Point out each Plasmodium parasite.
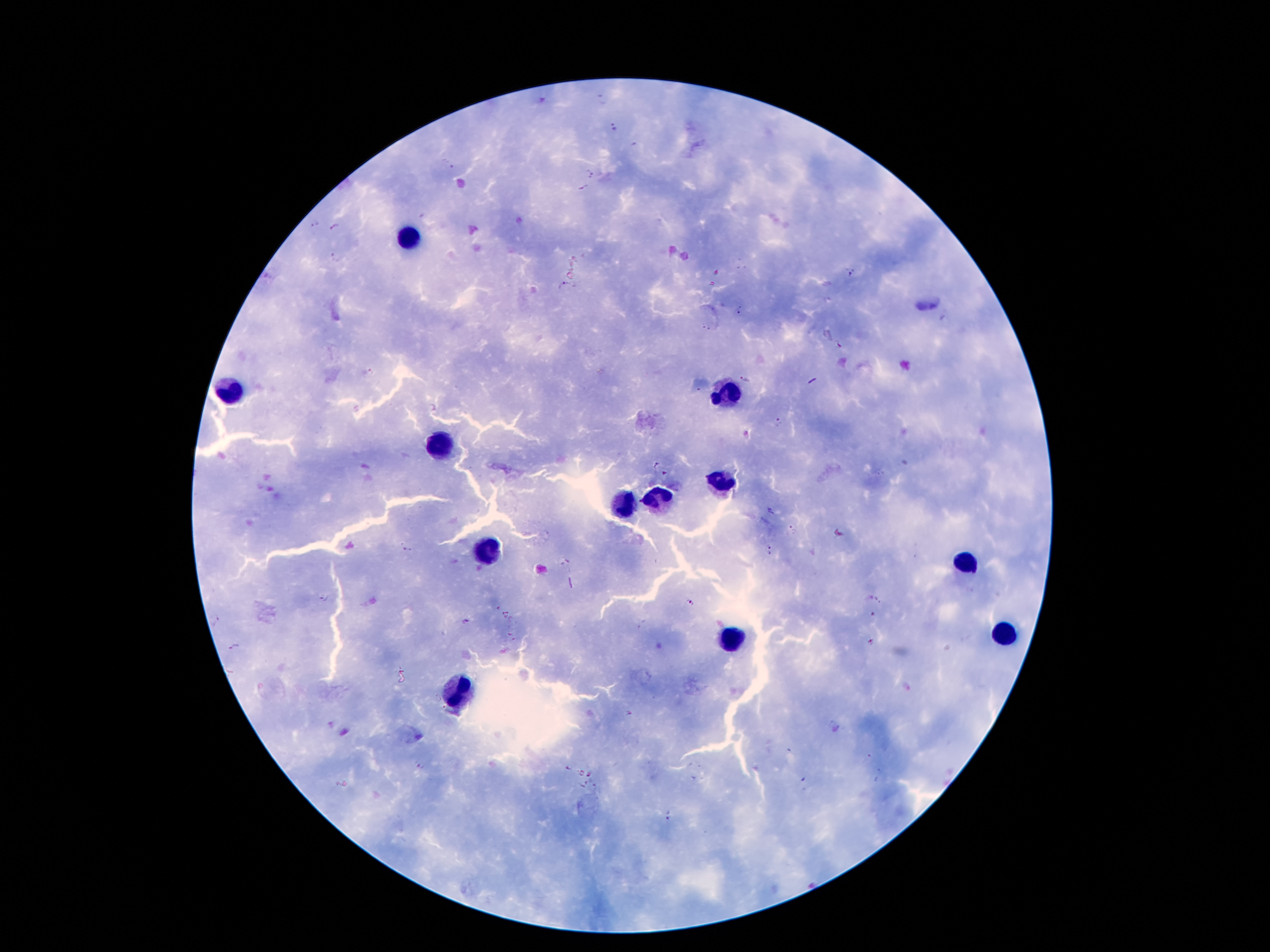

Approximate centers as {x, y} in pixels.
Plasmodium parasites: {601, 97}, {614, 127}, {589, 172}, {584, 189}, {315, 222}, {335, 227}, {337, 256}, {849, 271}, {565, 286}, {739, 311}, {707, 327}, {838, 345}, {743, 379}, {434, 408}, {779, 421}, {770, 511}, {791, 530}, {406, 549}, {770, 549}, {869, 598}, {877, 598}, {325, 599}, {690, 602}, {873, 614}, {214, 618}, {466, 622}, {872, 639}, {235, 646}, {906, 688}, {628, 714}, {329, 724}, {343, 732}, {868, 759}, {421, 766}, {568, 766}, {581, 772}, {589, 773}, {880, 777}, {803, 780}, {586, 782}, {596, 785}, {582, 786}, {669, 814}.

leukocyte locations = {410, 237}, {230, 391}, {722, 393}, {442, 449}, {720, 482}, {657, 499}, {622, 505}, {487, 552}, {965, 559}, {1002, 632}, {729, 636}, {456, 690}
capture = smartphone through the microscope eyepiece
patient malaria status = positive for Plasmodium falciparum
magnification = 100x
field of view = single
stain = Giemsa
image size = 1270×952 pixels
preparation = thick blood film